Assess this cell for malaria.
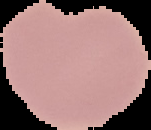

It is uninfected.

Summary:
  - Preparation: thin blood film
  - Image size: 151×130 pixels
  - Image type: segmented cell region with the area outside set to black